Locate every blood parasite and identify its species.
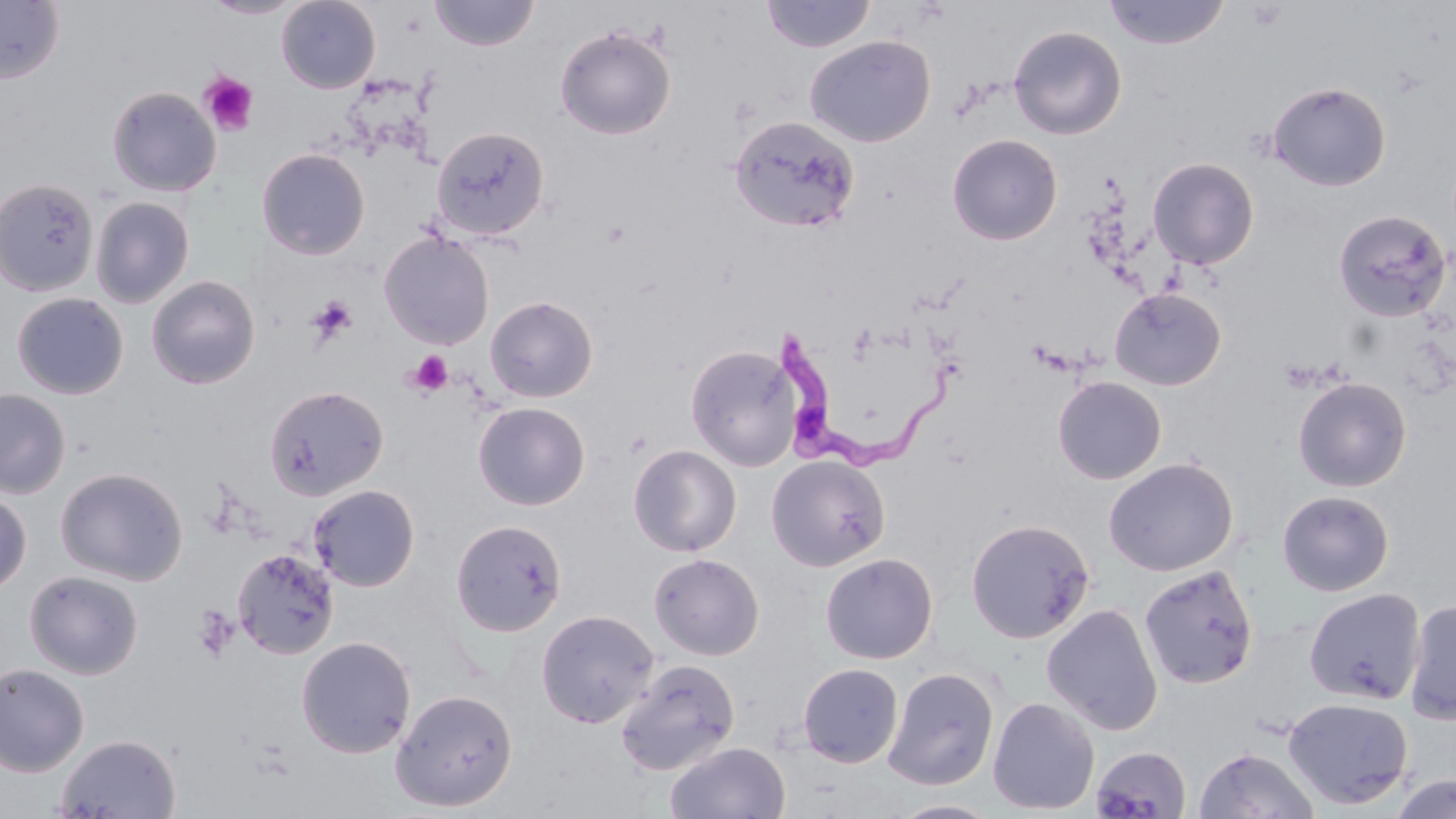
Approximate bounding boxes as (x1,y1)-(x2,y2) corner pairs in pixels.
Trypanosoma brucei: (774,329)-(956,481).
No Plasmodium falciparum, Plasmodium ovale, Plasmodium malariae, Plasmodium vivax, or Babesia divergens observed.

Summary:
  - Uninfected red blood cell locations: (0,0)-(65,85), (201,0)-(305,18), (277,0)-(380,93), (429,0)-(540,51), (760,0)-(876,53), (1103,0)-(1230,49), (554,24)-(676,140), (1008,25)-(1127,140), (805,35)-(936,147), (1267,81)-(1391,191), (106,86)-(221,196), (729,115)-(860,232), (431,125)-(551,242), (947,133)-(1063,245), (256,148)-(371,260), (1147,156)-(1259,270), (0,178)-(99,297), (90,196)-(195,308), (1333,209)-(1453,322), (378,231)-(495,350), (146,275)-(261,389), (1109,287)-(1227,391), (11,292)-(129,399), (485,295)-(599,403), (686,344)-(802,471), (1052,376)-(1167,484), (1292,376)-(1412,492), (263,384)-(389,501), (0,388)-(71,498), (473,402)-(590,510), (628,444)-(742,557), (766,454)-(891,571), (1103,457)-(1238,577), (55,467)-(188,585), (307,484)-(420,591), (1276,489)-(1395,597), (0,490)-(31,594), (450,518)-(567,637), (965,518)-(1094,644), (232,547)-(339,660), (819,552)-(938,664), (648,553)-(765,661), (1138,565)-(1259,689), (24,570)-(144,679), (1304,587)-(1426,705), (1404,597)-(1456,726), (1041,603)-(1163,735), (536,609)-(660,728), (296,636)-(417,758), (615,658)-(741,776), (0,663)-(89,777), (797,663)-(903,768), (883,667)-(1000,790), (390,688)-(519,811), (987,696)-(1100,815), (1282,696)-(1414,810), (55,733)-(180,818), (665,741)-(791,819), (1090,745)-(1192,819), (1194,746)-(1320,818), (1387,775)-(1456,818), (887,799)-(1003,818)
  - Platelet locations: (199,72)-(258,136), (306,296)-(357,346), (405,350)-(453,397), (192,605)-(240,660)
  - Slide-level diagnosis: Trypanosoma brucei
  - Preparation: thin blood film
  - Image size: 1456×819 pixels
  - Magnification: 1000x
  - Stain: May-Grünwald-Giemsa
  - Modality: optical microscopy
  - Field of view: single